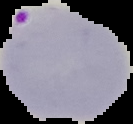
preparation = thin blood smear
malaria status = parasitized
image size = 133×124 pixels
image type = segmented cell region with the area outside set to black